Identify the cell.
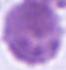

This is an erythrocyte.

Summary:
  - Magnification: 1000x
  - Modality: photomicrograph